Assess this cell for malaria.
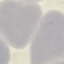
Uninfected.

Summary:
  - Image type: cell patch, automatically extracted from a larger field of view and resized to 64 × 64 pixels
  - Capture: smartphone camera at the microscope eyepiece
  - Preparation: thin blood smear
  - Stain: Giemsa